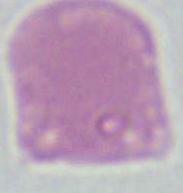

Summary:
  - Identification: red blood cell
  - Modality: photomicrograph
  - Magnification: 1000x